State which parasite is depicted.
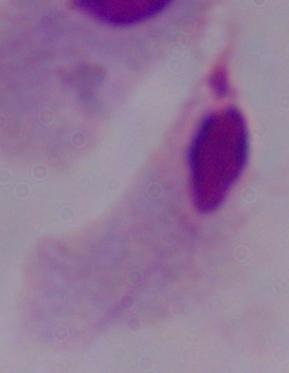

This is a trichomonad.

modality: micrograph
magnification: 1000x